Classify this cell by malaria status.
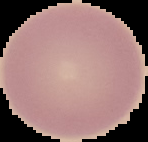
Uninfected.

{
  "image_size": "148×142 pixels",
  "preparation": "thin blood smear",
  "image_type": "segmented cell region on a black background"
}